Name the parasite shown.
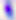

Toxoplasma gondii.

Captured at 400x magnification. Photomicrograph.